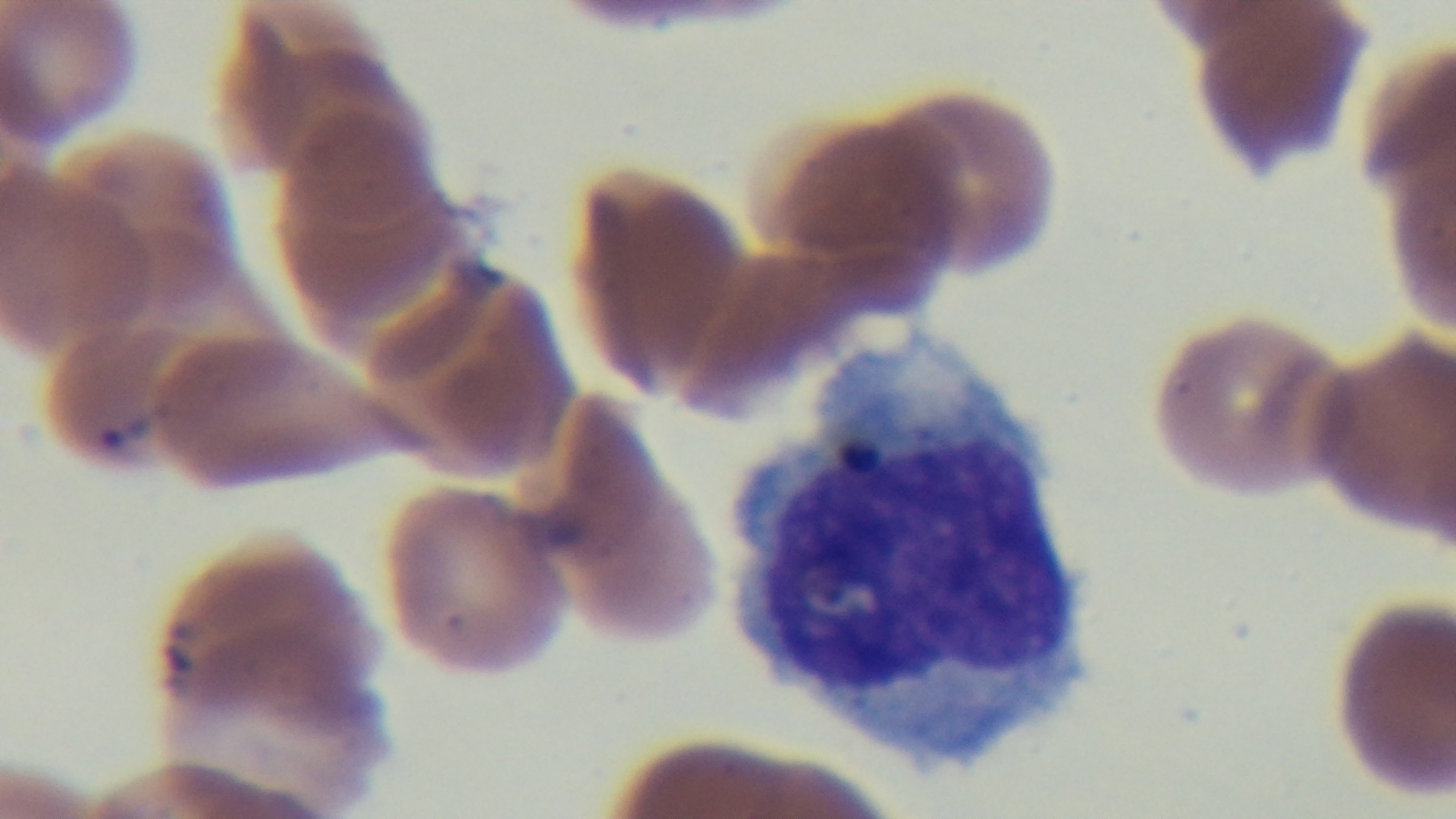
Summary:
  - Preparation: thin smear
  - Malaria status: positive
  - Field of view: one from the slide
  - Capture: mounted 4K digital camera
  - Objective: 100x oil immersion
  - Modality: light microscopy
  - Stain: Giemsa